State the blood parasite species.
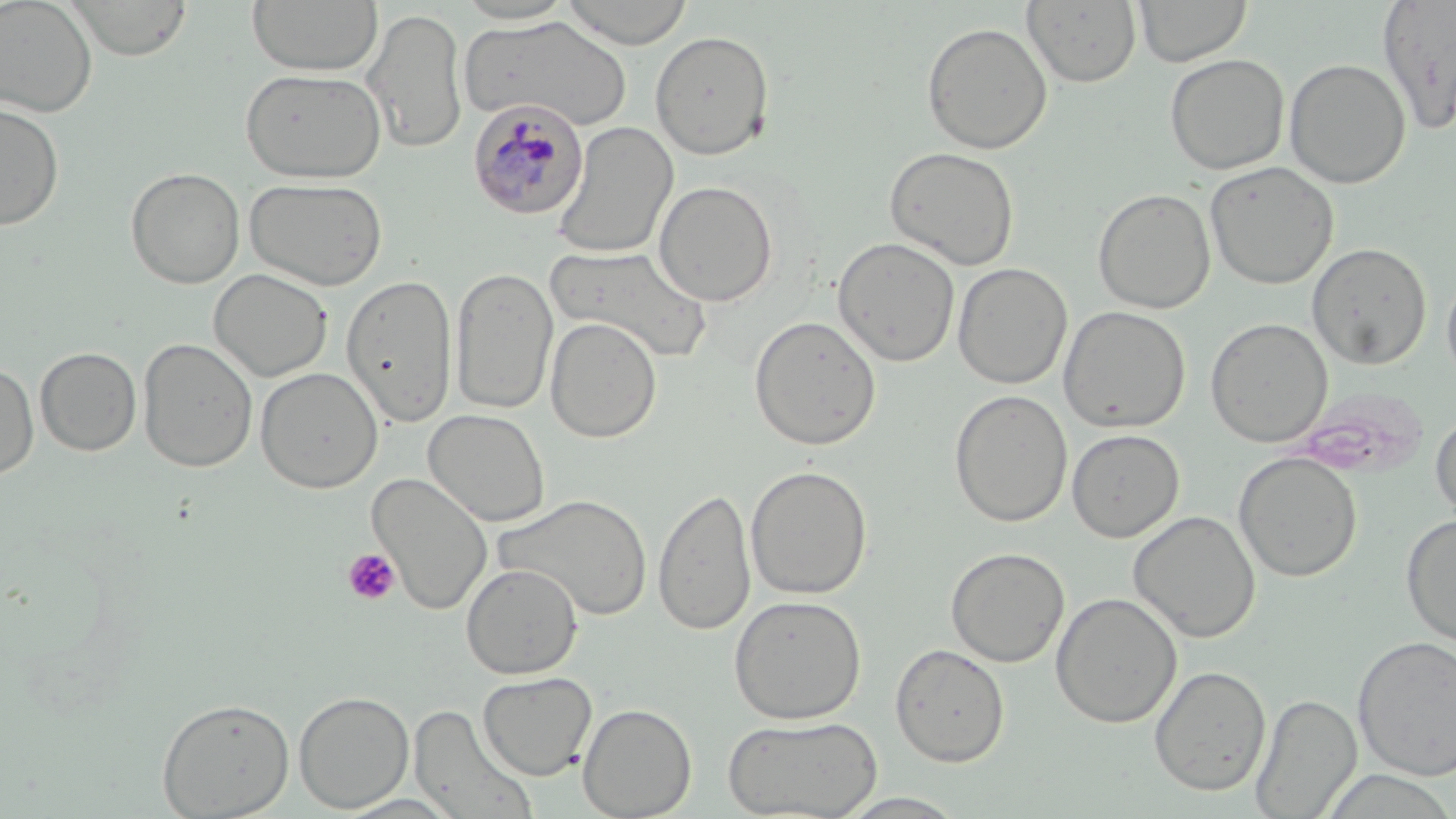

Plasmodium malariae.

{
  "platelet_locations": "approximate bounding boxes as named x1/y1/x2/y2 corners in pixels: (x1=342, y1=547, x2=401, y2=607)",
  "modality": "light microscopy",
  "uninfected_red_blood_cell_locations": "approximate bounding boxes as named x1/y1/x2/y2 corners in pixels: (x1=0, y1=0, x2=97, y2=117), (x1=68, y1=0, x2=192, y2=61), (x1=559, y1=0, x2=695, y2=48), (x1=1133, y1=0, x2=1252, y2=67), (x1=245, y1=1, x2=384, y2=76), (x1=451, y1=1, x2=578, y2=25), (x1=1022, y1=1, x2=1142, y2=88), (x1=1376, y1=1, x2=1455, y2=134), (x1=360, y1=7, x2=468, y2=155), (x1=462, y1=15, x2=632, y2=132), (x1=920, y1=22, x2=1053, y2=155), (x1=650, y1=29, x2=775, y2=160), (x1=1164, y1=53, x2=1290, y2=175), (x1=1284, y1=58, x2=1411, y2=189), (x1=240, y1=67, x2=386, y2=184), (x1=0, y1=100, x2=64, y2=232), (x1=551, y1=121, x2=678, y2=260), (x1=883, y1=146, x2=1020, y2=271), (x1=1204, y1=161, x2=1339, y2=290), (x1=125, y1=166, x2=245, y2=289), (x1=245, y1=177, x2=388, y2=291), (x1=653, y1=180, x2=779, y2=307), (x1=1092, y1=187, x2=1216, y2=314), (x1=832, y1=236, x2=961, y2=367), (x1=1306, y1=242, x2=1432, y2=370), (x1=547, y1=245, x2=712, y2=364), (x1=952, y1=263, x2=1073, y2=390), (x1=450, y1=266, x2=558, y2=416), (x1=209, y1=268, x2=333, y2=383), (x1=1441, y1=269, x2=1456, y2=389), (x1=341, y1=272, x2=458, y2=427), (x1=1058, y1=305, x2=1191, y2=433), (x1=749, y1=315, x2=882, y2=451), (x1=545, y1=317, x2=663, y2=443), (x1=1205, y1=317, x2=1332, y2=448), (x1=138, y1=336, x2=258, y2=473), (x1=35, y1=346, x2=142, y2=457), (x1=0, y1=361, x2=39, y2=481), (x1=255, y1=367, x2=383, y2=493), (x1=949, y1=390, x2=1073, y2=527), (x1=423, y1=409, x2=551, y2=527), (x1=1430, y1=410, x2=1456, y2=525), (x1=1067, y1=429, x2=1184, y2=542), (x1=1233, y1=452, x2=1362, y2=583), (x1=744, y1=465, x2=873, y2=600), (x1=367, y1=471, x2=493, y2=615), (x1=653, y1=487, x2=756, y2=635), (x1=493, y1=493, x2=654, y2=621), (x1=1127, y1=509, x2=1261, y2=643), (x1=1400, y1=514, x2=1456, y2=646), (x1=945, y1=546, x2=1070, y2=668), (x1=461, y1=563, x2=583, y2=679), (x1=1050, y1=592, x2=1182, y2=729), (x1=729, y1=594, x2=867, y2=724), (x1=1352, y1=635, x2=1456, y2=781), (x1=889, y1=643, x2=1010, y2=767), (x1=1149, y1=665, x2=1271, y2=797), (x1=477, y1=671, x2=598, y2=780), (x1=293, y1=690, x2=414, y2=812), (x1=1250, y1=693, x2=1362, y2=818), (x1=156, y1=697, x2=295, y2=818), (x1=577, y1=702, x2=697, y2=819), (x1=408, y1=704, x2=540, y2=818), (x1=723, y1=715, x2=882, y2=819), (x1=1318, y1=769, x2=1456, y2=818), (x1=834, y1=791, x2=971, y2=817), (x1=331, y1=793, x2=466, y2=818)",
  "stain": "May-Grünwald-Giemsa",
  "field_of_view": "one of a larger specimen",
  "image_size": "1456×819 pixels",
  "preparation": "thin blood film",
  "magnification": "1000x",
  "plasmodium_malariae_infected_red_blood_cell_locations": "approximate bounding boxes as named x1/y1/x2/y2 corners in pixels: (x1=468, y1=98, x2=589, y2=221)"
}